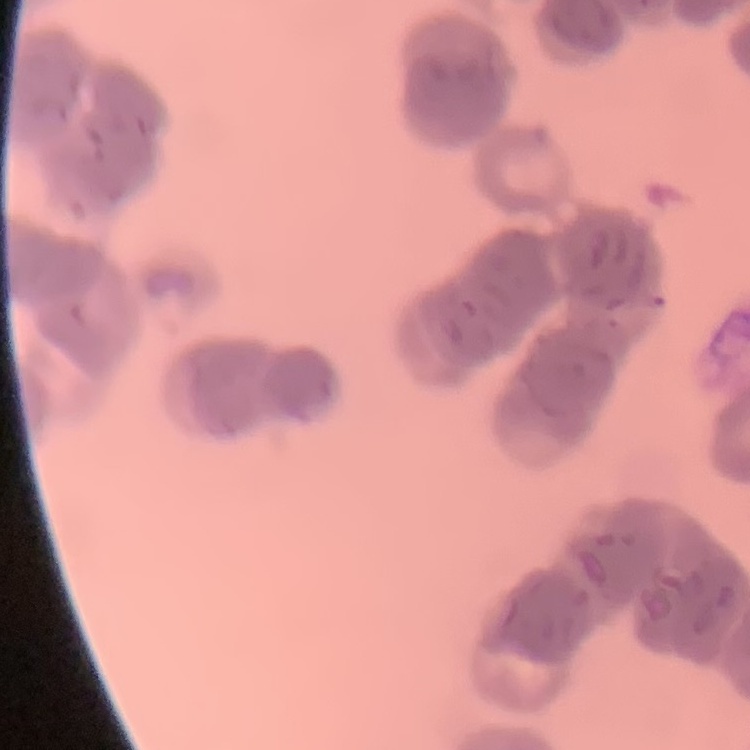

The red blood cells exhibit rouleaux formation. Field's or Giemsa stain. One tile cut from a larger photomicrograph. Thin peripheral smear.